Assess the morphology of the red blood cells.
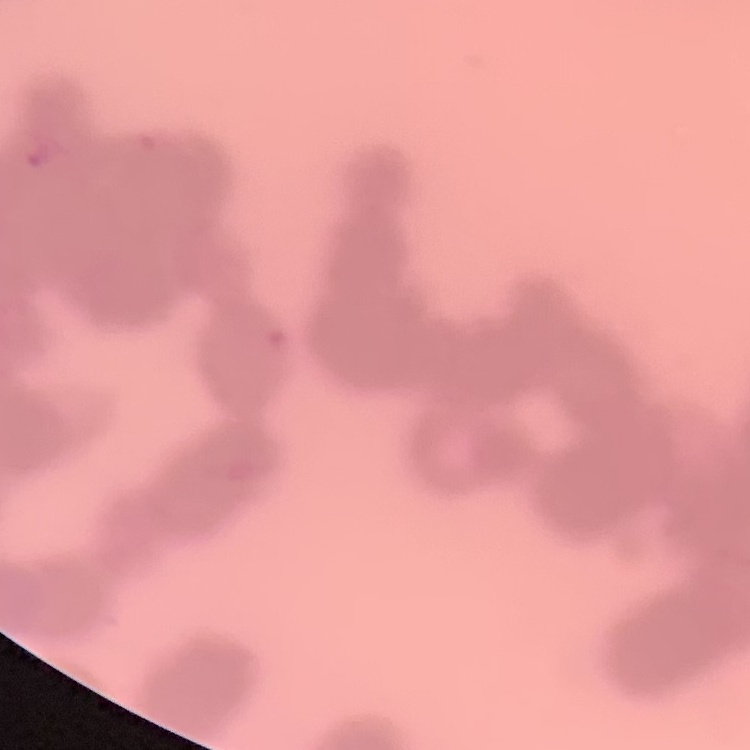
They show rouleaux formation.

Field's or Giemsa stain. Thin peripheral smear. Square crop of a larger photomicrograph.